Name the parasite shown.
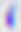
Toxoplasma gondii.

400x magnification. Micrograph.